Report the malaria status of this cell.
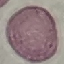
Uninfected.

image type = automatically extracted cell patch, resized to 64 × 64 pixels
stain = Giemsa
capture = smartphone camera at the microscope eyepiece
preparation = thin blood smear